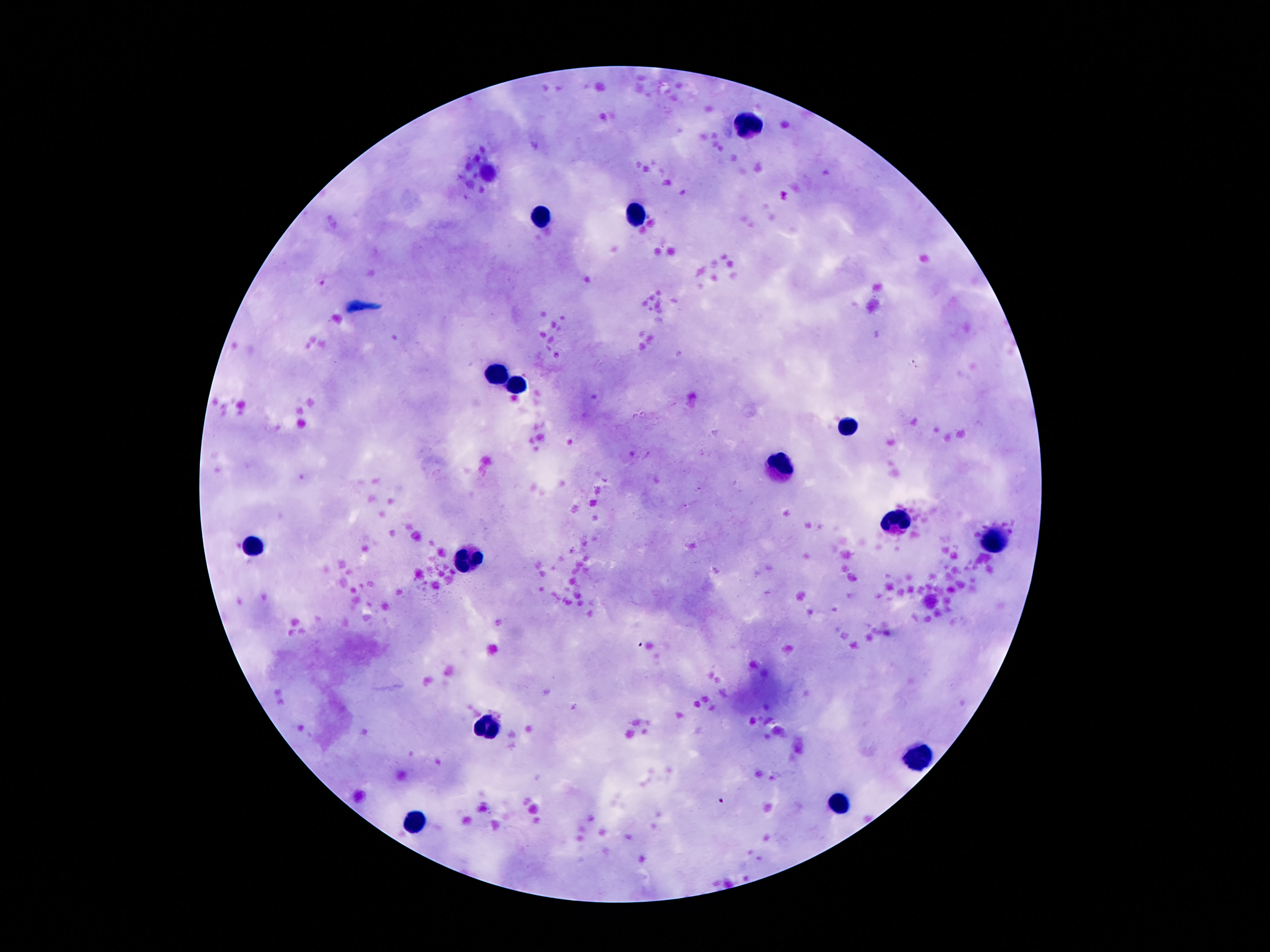
Approximate centers as (x, y) in pixels. Leukocyte locations: (749, 127), (636, 217), (540, 219), (497, 376), (520, 387), (849, 428), (785, 466), (896, 524), (994, 541), (252, 548), (468, 558), (486, 728), (922, 757), (844, 803), (418, 821). Thick peripheral-blood smear. Patient malaria status: not infected. 100x magnification. Giemsa-stained preparation. Image is 1270×952 pixels. Photographed through the microscope eyepiece with a smartphone camera. One field from this slide.